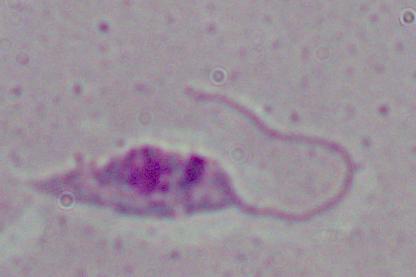

Photomicrograph. A Leishmania parasite is shown. 1000x magnification.